Locate and identify every blood parasite.
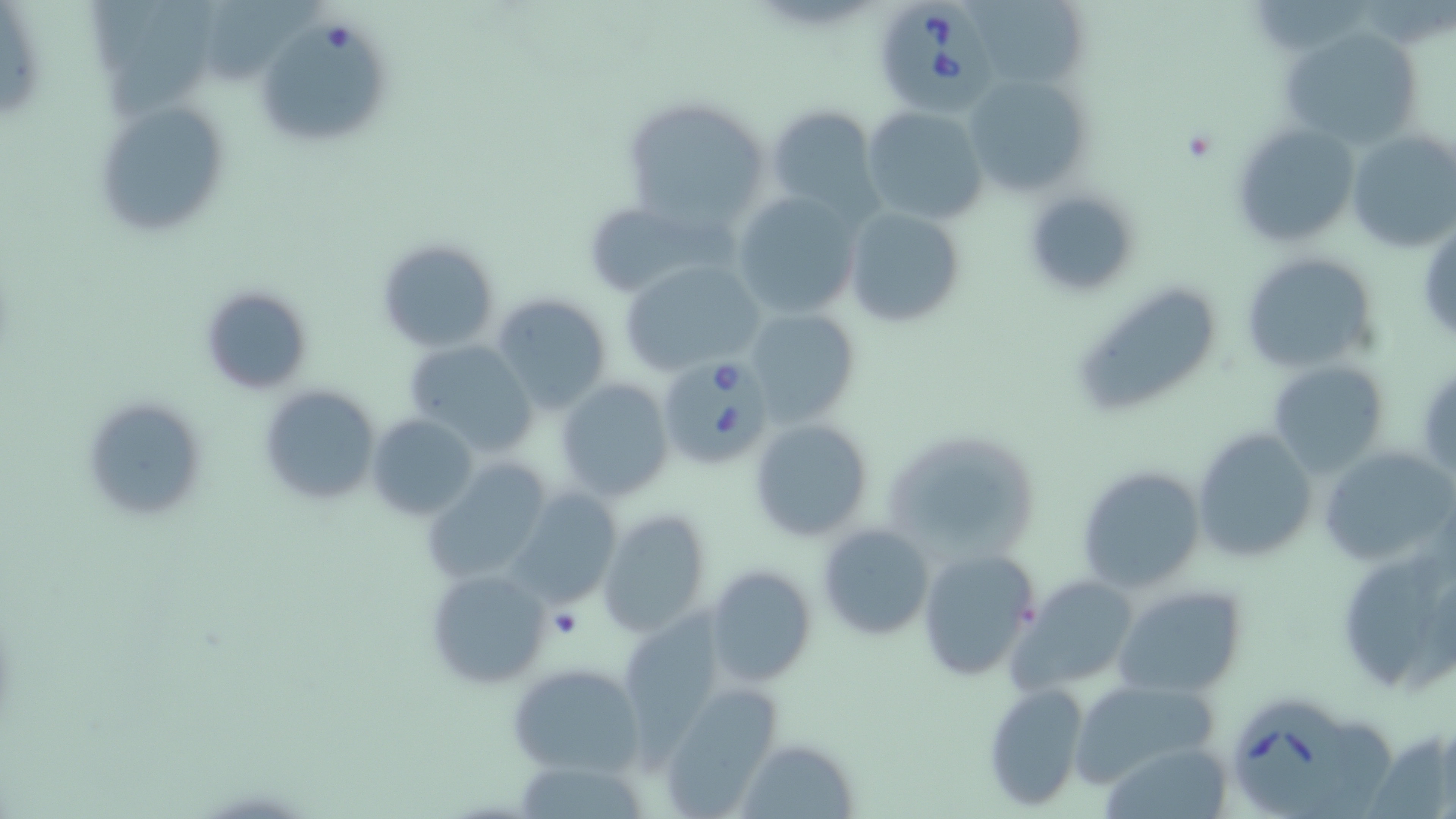

Approximate bounding boxes as named x1/y1/x2/y2 corners in pixels.
Babesia divergens-infected red blood cells: (x1=869, y1=1, x2=994, y2=115), (x1=655, y1=359, x2=769, y2=474), (x1=1234, y1=698, x2=1354, y2=813).
No Plasmodium falciparum, Plasmodium ovale, Plasmodium malariae, Plasmodium vivax, or Trypanosoma brucei observed.

Platelet locations: (x1=1181, y1=129, x2=1214, y2=161). Uninfected red blood cell locations: (x1=971, y1=0, x2=1091, y2=92), (x1=104, y1=1, x2=237, y2=120), (x1=203, y1=3, x2=318, y2=83), (x1=264, y1=24, x2=394, y2=141), (x1=1279, y1=24, x2=1424, y2=149), (x1=962, y1=69, x2=1096, y2=197), (x1=619, y1=97, x2=774, y2=231), (x1=94, y1=99, x2=231, y2=235), (x1=766, y1=105, x2=881, y2=217), (x1=862, y1=106, x2=988, y2=227), (x1=1230, y1=122, x2=1356, y2=246), (x1=1347, y1=127, x2=1456, y2=253), (x1=1023, y1=188, x2=1139, y2=295), (x1=731, y1=191, x2=861, y2=320), (x1=843, y1=205, x2=966, y2=329), (x1=591, y1=206, x2=748, y2=300), (x1=375, y1=239, x2=500, y2=353), (x1=1240, y1=251, x2=1378, y2=373), (x1=619, y1=256, x2=766, y2=375), (x1=1068, y1=282, x2=1225, y2=420), (x1=199, y1=284, x2=312, y2=396), (x1=492, y1=291, x2=612, y2=413), (x1=743, y1=308, x2=861, y2=428), (x1=403, y1=339, x2=540, y2=456), (x1=1268, y1=360, x2=1390, y2=479), (x1=554, y1=379, x2=673, y2=502), (x1=257, y1=383, x2=381, y2=508), (x1=79, y1=394, x2=206, y2=523), (x1=367, y1=413, x2=479, y2=520), (x1=749, y1=418, x2=874, y2=541), (x1=881, y1=427, x2=1043, y2=561), (x1=1193, y1=427, x2=1318, y2=565), (x1=1315, y1=442, x2=1456, y2=570), (x1=423, y1=459, x2=553, y2=585), (x1=1079, y1=465, x2=1204, y2=592), (x1=507, y1=487, x2=623, y2=604), (x1=596, y1=509, x2=712, y2=638), (x1=816, y1=523, x2=935, y2=641), (x1=914, y1=547, x2=1040, y2=682), (x1=1337, y1=555, x2=1448, y2=701), (x1=704, y1=564, x2=816, y2=689), (x1=427, y1=568, x2=554, y2=689), (x1=1013, y1=578, x2=1140, y2=695), (x1=1111, y1=581, x2=1248, y2=700), (x1=623, y1=596, x2=730, y2=778), (x1=505, y1=662, x2=642, y2=777), (x1=1068, y1=677, x2=1221, y2=789), (x1=983, y1=682, x2=1090, y2=810), (x1=661, y1=685, x2=783, y2=815), (x1=734, y1=738, x2=858, y2=817), (x1=1096, y1=749, x2=1230, y2=819), (x1=513, y1=758, x2=656, y2=819). Slide-level diagnosis: Babesia divergens. Image is 1456×819 pixels. One field of a larger specimen. May-Grünwald-Giemsa-stained preparation. Light microscopy. Thin blood film. Captured at 1000x magnification.